Locate every malaria parasite and every leukocyte.
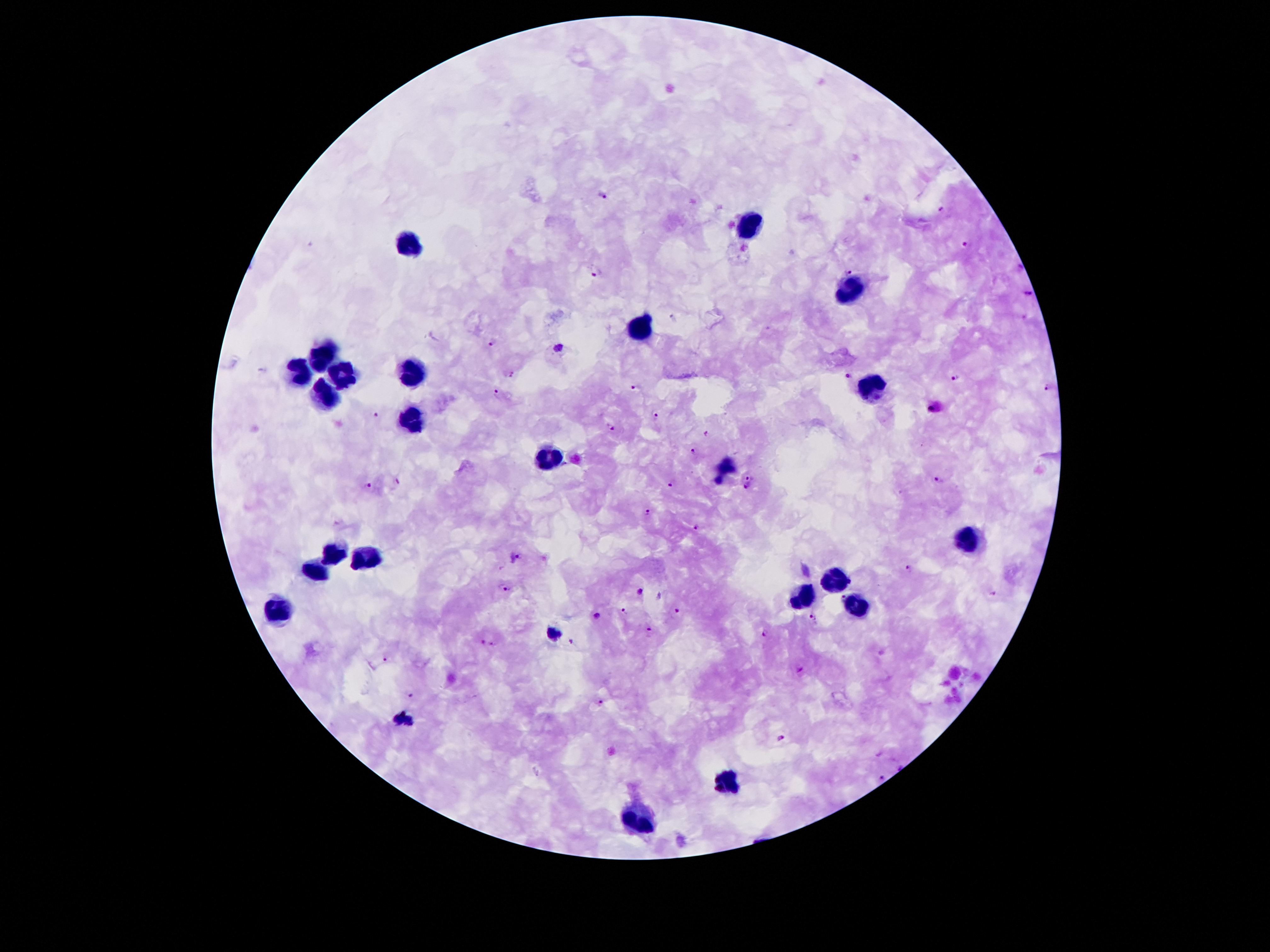
Approximate centers as (x, y) in pixels.
Malaria parasites: (605, 193), (944, 210), (962, 246), (1019, 268), (849, 270), (594, 272), (1027, 294), (673, 319), (488, 342), (560, 346), (263, 370), (511, 372), (850, 377), (955, 378), (636, 386), (1046, 389), (498, 390), (932, 407), (375, 416), (655, 416), (611, 426), (705, 433), (693, 449), (751, 477), (940, 479), (397, 480), (369, 483), (672, 485), (746, 487), (646, 512), (697, 529), (520, 555), (908, 569), (507, 589), (640, 590), (991, 592), (660, 596), (843, 597), (624, 610), (678, 610), (599, 616), (813, 617), (649, 628), (552, 633), (764, 633), (570, 640), (482, 642), (494, 644), (384, 658), (801, 669), (410, 696), (602, 702), (405, 720), (781, 740), (880, 777).
Leukocytes: (755, 222), (410, 242), (849, 294), (641, 325), (324, 357), (410, 371), (299, 374), (341, 374), (326, 391), (870, 392), (408, 418), (549, 458), (969, 539), (332, 554), (364, 554), (316, 576), (834, 577), (803, 590), (853, 607), (274, 609), (727, 784), (641, 819).

Summary:
  - Patient malaria status: infected with Plasmodium falciparum
  - Stain: Giemsa
  - Preparation: thick blood smear
  - Image size: 1270×952 pixels
  - Magnification: 100x
  - Field of view: one from this slide
  - Capture: smartphone through the microscope eyepiece